Locate and identify every blood parasite.
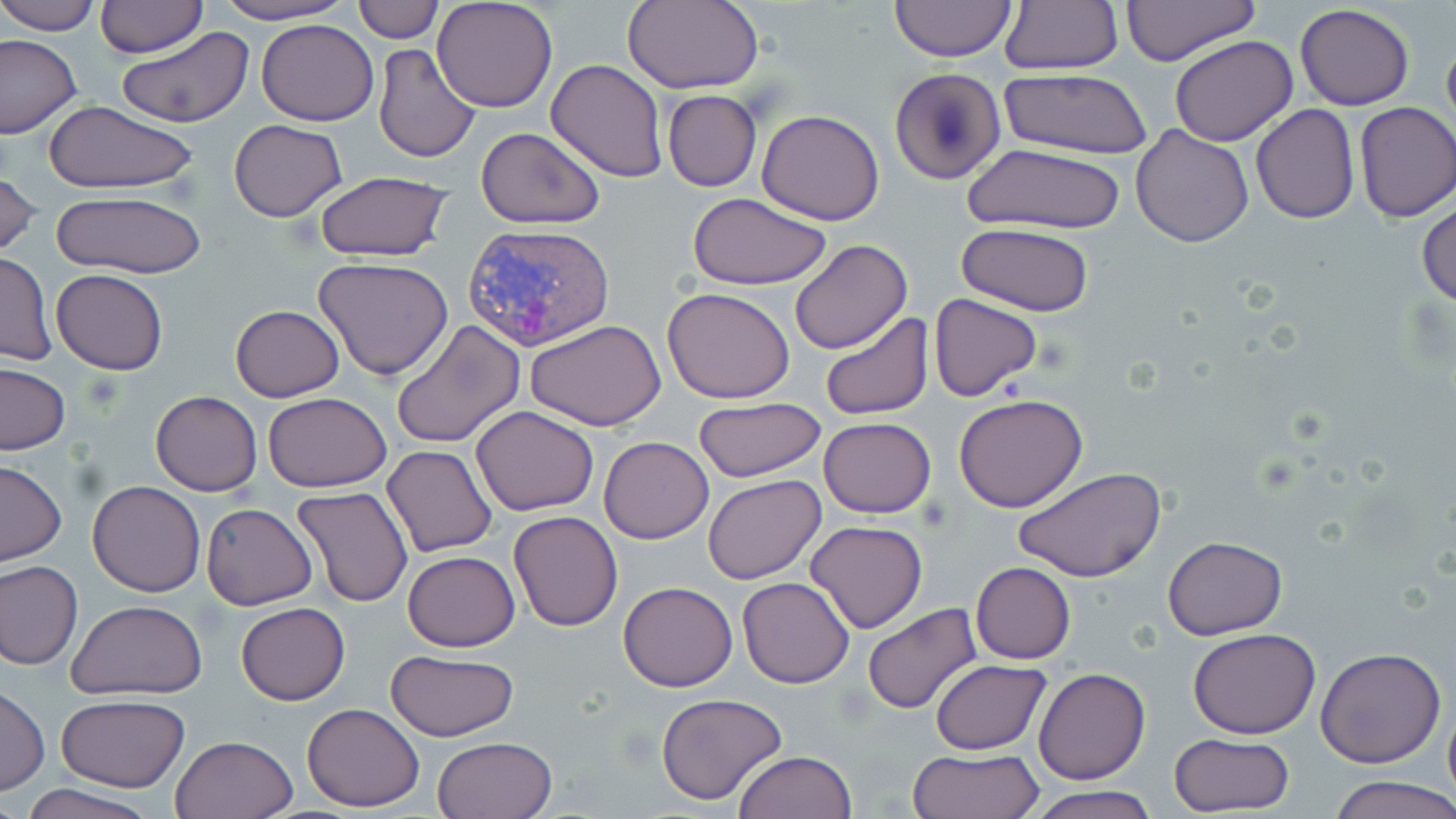
Approximate bounding boxes as named x1/y1/x2/y2 corners in pixels.
Plasmodium vivax-infected red blood cells: (x1=463, y1=222, x2=616, y2=351).
No Plasmodium falciparum, Plasmodium ovale, Plasmodium malariae, Babesia divergens, or Trypanosoma brucei observed.

slide_level_diagnosis: Plasmodium vivax
preparation: thin blood smear
uninfected_red_blood_cell_locations: 'approximate bounding boxes as named x1/y1/x2/y2 corners in pixels: (x1=0, y1=0, x2=102, y2=35), (x1=207, y1=0, x2=355, y2=25), (x1=353, y1=0, x2=442, y2=43), (x1=432, y1=0, x2=560, y2=112), (x1=888, y1=0, x2=1017, y2=63), (x1=1000, y1=0, x2=1123, y2=75), (x1=1121, y1=0, x2=1261, y2=67), (x1=622, y1=1, x2=764, y2=92), (x1=94, y1=2, x2=207, y2=58), (x1=1295, y1=3, x2=1415, y2=111), (x1=256, y1=18, x2=379, y2=126), (x1=1441, y1=26, x2=1456, y2=144), (x1=118, y1=27, x2=254, y2=128), (x1=0, y1=33, x2=83, y2=138), (x1=1168, y1=35, x2=1298, y2=147), (x1=373, y1=43, x2=483, y2=165), (x1=547, y1=59, x2=667, y2=181), (x1=890, y1=67, x2=1007, y2=185), (x1=1000, y1=69, x2=1152, y2=159), (x1=662, y1=89, x2=762, y2=192), (x1=43, y1=100, x2=197, y2=196), (x1=1354, y1=102, x2=1455, y2=222), (x1=1251, y1=105, x2=1360, y2=223), (x1=757, y1=109, x2=885, y2=225), (x1=228, y1=119, x2=348, y2=221), (x1=1131, y1=124, x2=1255, y2=248), (x1=475, y1=126, x2=605, y2=230), (x1=961, y1=142, x2=1127, y2=236), (x1=0, y1=168, x2=41, y2=263), (x1=313, y1=172, x2=453, y2=262), (x1=51, y1=190, x2=206, y2=277), (x1=687, y1=193, x2=833, y2=290), (x1=1418, y1=194, x2=1456, y2=308), (x1=956, y1=224, x2=1098, y2=316), (x1=788, y1=239, x2=912, y2=353), (x1=0, y1=251, x2=56, y2=366), (x1=314, y1=256, x2=455, y2=381), (x1=51, y1=269, x2=167, y2=375), (x1=663, y1=287, x2=796, y2=403), (x1=930, y1=293, x2=1041, y2=403), (x1=230, y1=304, x2=345, y2=401), (x1=819, y1=312, x2=935, y2=422), (x1=392, y1=319, x2=526, y2=450), (x1=525, y1=320, x2=666, y2=430), (x1=1, y1=363, x2=71, y2=454), (x1=150, y1=390, x2=261, y2=495), (x1=264, y1=392, x2=391, y2=492), (x1=954, y1=392, x2=1089, y2=512), (x1=691, y1=397, x2=827, y2=484), (x1=470, y1=405, x2=600, y2=516), (x1=819, y1=417, x2=936, y2=518), (x1=599, y1=436, x2=714, y2=544), (x1=382, y1=445, x2=496, y2=558), (x1=0, y1=459, x2=66, y2=566), (x1=1013, y1=465, x2=1168, y2=583), (x1=703, y1=475, x2=826, y2=585), (x1=88, y1=480, x2=204, y2=597), (x1=293, y1=485, x2=413, y2=607), (x1=201, y1=501, x2=318, y2=610), (x1=508, y1=510, x2=623, y2=632), (x1=805, y1=520, x2=928, y2=634), (x1=1162, y1=537, x2=1288, y2=638), (x1=402, y1=550, x2=519, y2=652), (x1=0, y1=561, x2=83, y2=670), (x1=970, y1=562, x2=1076, y2=664), (x1=737, y1=575, x2=855, y2=689), (x1=618, y1=581, x2=739, y2=691), (x1=68, y1=600, x2=208, y2=701), (x1=236, y1=603, x2=350, y2=705), (x1=863, y1=604, x2=981, y2=714), (x1=1188, y1=628, x2=1320, y2=739), (x1=1315, y1=645, x2=1447, y2=768), (x1=386, y1=650, x2=518, y2=742), (x1=928, y1=658, x2=1052, y2=754), (x1=1034, y1=667, x2=1150, y2=785), (x1=0, y1=685, x2=48, y2=795), (x1=655, y1=692, x2=790, y2=807), (x1=1443, y1=694, x2=1456, y2=810), (x1=57, y1=695, x2=188, y2=791), (x1=302, y1=702, x2=425, y2=812), (x1=1167, y1=733, x2=1295, y2=817), (x1=170, y1=734, x2=297, y2=818), (x1=432, y1=736, x2=557, y2=819), (x1=909, y1=746, x2=1044, y2=819), (x1=732, y1=751, x2=857, y2=819), (x1=1332, y1=776, x2=1456, y2=819), (x1=21, y1=784, x2=155, y2=819), (x1=1024, y1=786, x2=1162, y2=819)'
image_size: 1456×819 pixels
stain: May-Grünwald-Giemsa
modality: light microscopy
magnification: 1000x
field_of_view: single